Classify this cell by malaria status.
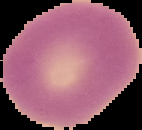

It is uninfected.

Summary:
  - Preparation: thin blood film
  - Image size: 142×130 pixels
  - Image type: cell region segmented out of the field of view; surrounding area masked to black